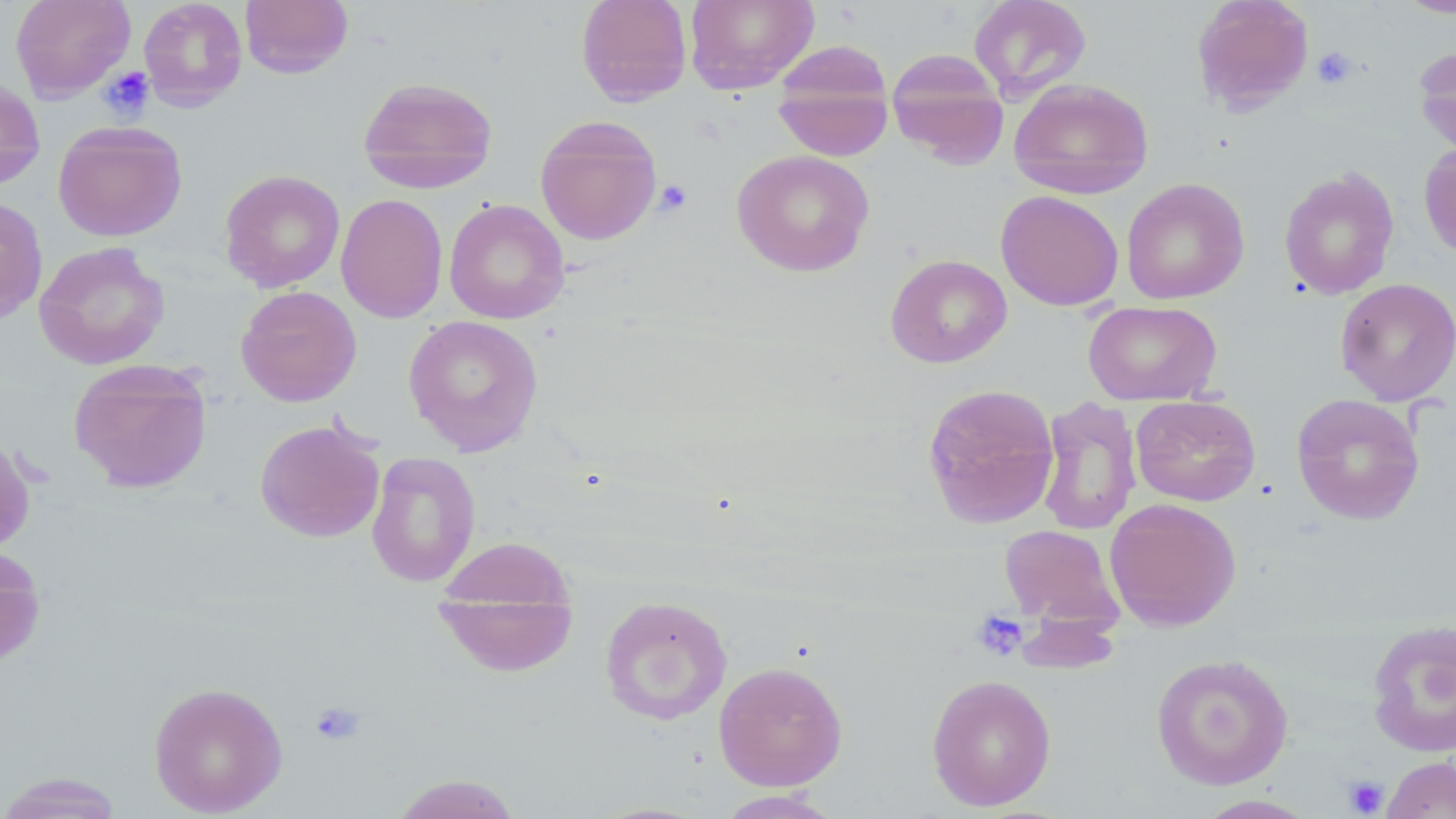
slide_level_diagnosis: no evidence of blood parasites
preparation: thin blood film
stain: May-Grünwald-Giemsa
modality: optical microscopy
magnification: 1000x
platelet_locations: 'approximate bounding boxes as [x1, y1, x2, y2] in pixels: [1312, 46, 1358, 89], [99, 66, 155, 122], [654, 179, 693, 217], [972, 610, 1029, 661], [309, 701, 366, 746], [1344, 775, 1389, 816]'
uninfected_red_blood_cell_locations: 'approximate bounding boxes as [x1, y1, x2, y2] in pixels: [10, 0, 135, 101], [138, 0, 247, 111], [239, 0, 354, 79], [575, 0, 692, 105], [685, 0, 819, 94], [968, 0, 1092, 101], [1191, 0, 1314, 114], [1395, 0, 1456, 18], [771, 40, 894, 160], [1414, 43, 1456, 159], [887, 48, 1010, 167], [0, 77, 46, 191], [358, 77, 498, 192], [1009, 78, 1154, 198], [535, 115, 663, 245], [52, 120, 187, 242], [1418, 142, 1456, 259], [731, 149, 875, 277], [1278, 167, 1399, 300], [219, 170, 345, 292], [1121, 178, 1250, 305], [995, 190, 1124, 311], [336, 193, 448, 323], [0, 197, 48, 324], [444, 199, 570, 324], [34, 241, 170, 370], [885, 254, 1012, 368], [1334, 277, 1456, 406], [235, 286, 362, 406], [1083, 300, 1222, 406], [403, 315, 544, 456], [68, 358, 213, 494], [922, 383, 1060, 529], [1291, 393, 1424, 526], [1131, 395, 1261, 506], [1036, 396, 1143, 537], [255, 419, 385, 543], [0, 436, 36, 557], [366, 452, 481, 588], [1104, 498, 1242, 631], [999, 524, 1124, 630], [432, 537, 580, 676], [0, 547, 46, 667], [599, 595, 732, 725], [1366, 618, 1456, 757], [1150, 652, 1294, 790], [713, 661, 848, 791], [926, 674, 1056, 811], [148, 681, 288, 817], [1381, 756, 1456, 818], [0, 773, 126, 818], [388, 773, 523, 818], [714, 789, 847, 818], [1193, 795, 1320, 818]'
field_of_view: one of a larger specimen
image_size: 1456×819 pixels